Assess this cell for malaria.
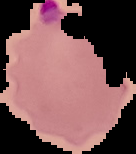
It is parasitized.

From a thin blood smear. Cell region segmented out of the field of view; the surrounding area is masked to black. Image is 136×154 pixels.